Assess the morphology of the erythrocytes.
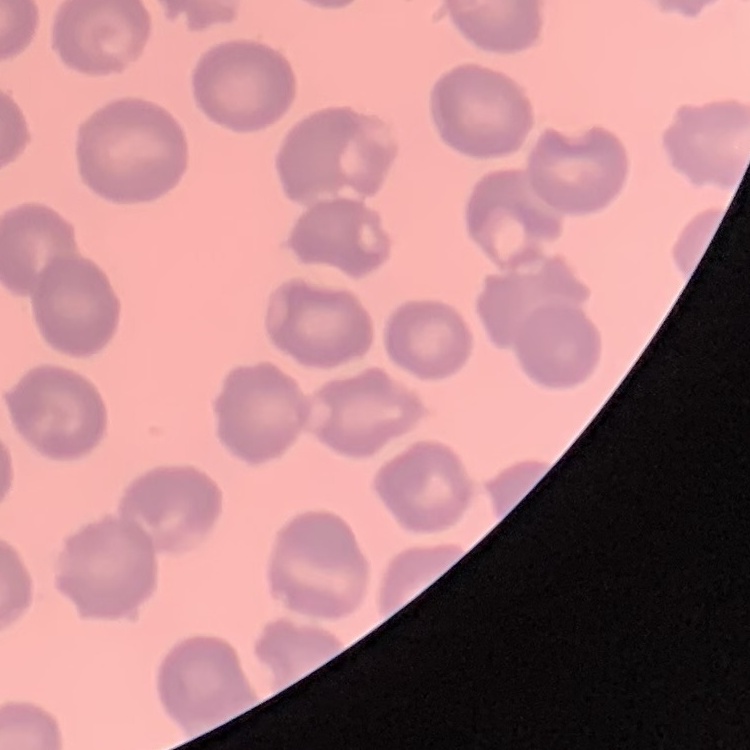
They show no rouleaux formation.

Stained with either Field's or Giemsa. Square crop of a larger photomicrograph. Thin peripheral smear.